Classify this cell by malaria status.
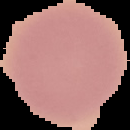

Uninfected.

preparation = thin blood film
image size = 130×130 pixels
image type = cell region segmented out of the field of view; surrounding area masked to black